Identify the blood parasite species.
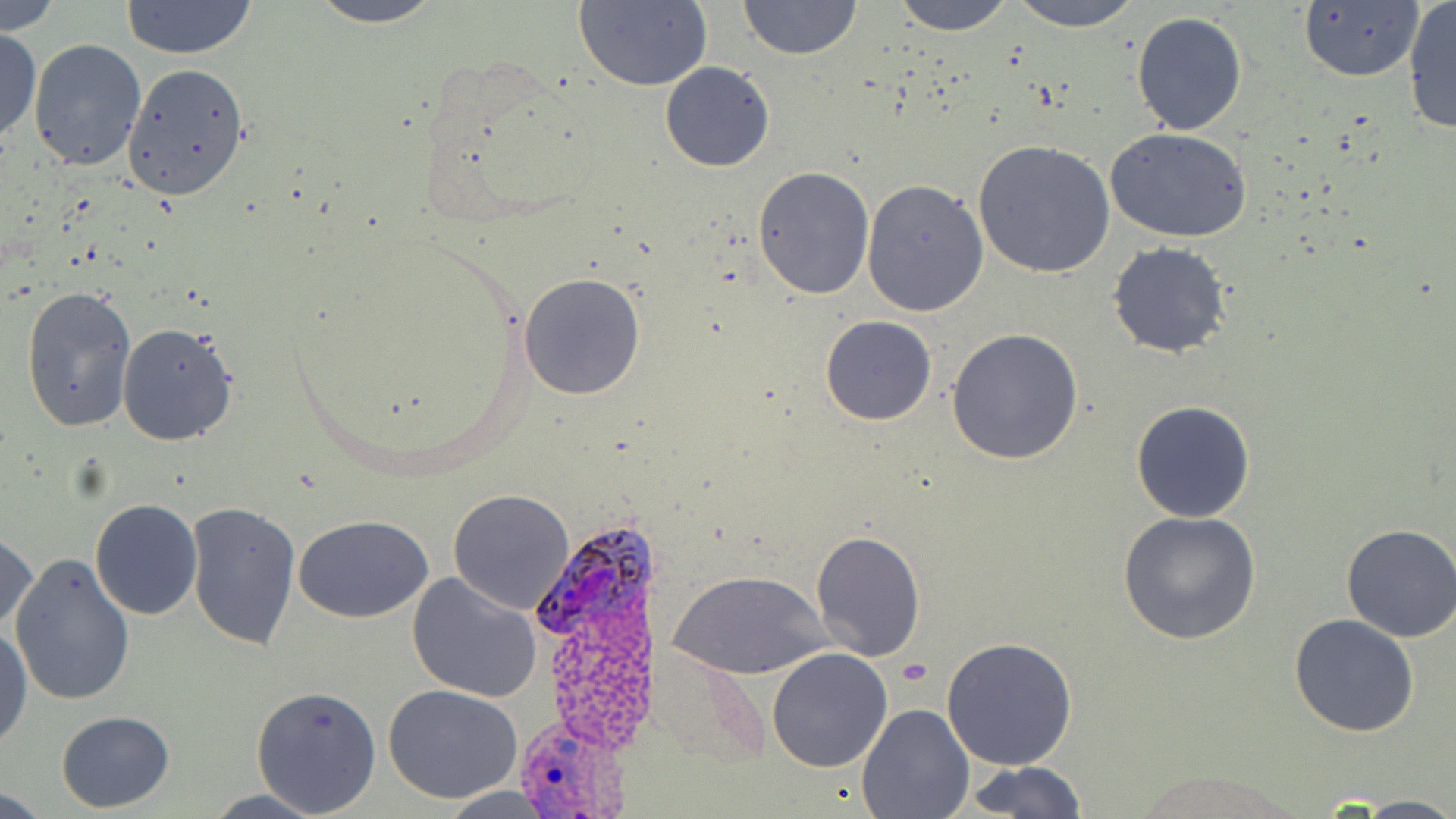
Plasmodium ovale.

{
  "stain": "May-Grünwald-Giemsa",
  "plasmodium_ovale_infected_red_blood_cell_locations": "approximate bounding boxes as named x1/y1/x2/y2 corners in pixels: (x1=534, y1=528, x2=655, y2=640), (x1=512, y1=716, x2=630, y2=819)",
  "image_size": "1456×819 pixels",
  "uninfected_red_blood_cell_locations": "approximate bounding boxes as named x1/y1/x2/y2 corners in pixels: (x1=119, y1=0, x2=259, y2=60), (x1=305, y1=0, x2=447, y2=28), (x1=892, y1=0, x2=1015, y2=36), (x1=1005, y1=0, x2=1146, y2=30), (x1=1, y1=1, x2=63, y2=35), (x1=738, y1=1, x2=862, y2=59), (x1=1402, y1=1, x2=1456, y2=136), (x1=573, y1=2, x2=713, y2=91), (x1=1297, y1=3, x2=1424, y2=84), (x1=1131, y1=10, x2=1248, y2=136), (x1=0, y1=27, x2=41, y2=147), (x1=27, y1=39, x2=146, y2=173), (x1=659, y1=61, x2=775, y2=172), (x1=120, y1=62, x2=251, y2=201), (x1=1107, y1=129, x2=1253, y2=242), (x1=971, y1=140, x2=1115, y2=279), (x1=752, y1=166, x2=874, y2=299), (x1=861, y1=180, x2=989, y2=315), (x1=1107, y1=241, x2=1233, y2=357), (x1=518, y1=273, x2=645, y2=400), (x1=21, y1=286, x2=138, y2=432), (x1=820, y1=315, x2=937, y2=425), (x1=116, y1=320, x2=239, y2=447), (x1=946, y1=328, x2=1083, y2=466), (x1=1131, y1=399, x2=1256, y2=522), (x1=447, y1=489, x2=575, y2=613), (x1=91, y1=498, x2=203, y2=619), (x1=185, y1=500, x2=301, y2=653), (x1=1118, y1=512, x2=1261, y2=646), (x1=294, y1=515, x2=434, y2=623), (x1=1338, y1=525, x2=1456, y2=642), (x1=1, y1=530, x2=38, y2=637), (x1=810, y1=531, x2=926, y2=661), (x1=9, y1=552, x2=134, y2=705), (x1=671, y1=568, x2=831, y2=678), (x1=406, y1=571, x2=545, y2=703), (x1=1289, y1=614, x2=1421, y2=736), (x1=0, y1=623, x2=31, y2=750), (x1=941, y1=637, x2=1077, y2=771), (x1=766, y1=647, x2=894, y2=773), (x1=249, y1=684, x2=381, y2=815), (x1=383, y1=684, x2=525, y2=805), (x1=856, y1=702, x2=975, y2=818), (x1=57, y1=711, x2=175, y2=811), (x1=962, y1=760, x2=1088, y2=819), (x1=1129, y1=767, x2=1305, y2=819), (x1=203, y1=790, x2=328, y2=819), (x1=1355, y1=795, x2=1456, y2=818)",
  "preparation": "thin blood smear",
  "modality": "light microscopy",
  "field_of_view": "one of a larger specimen",
  "magnification": "1000x",
  "platelet_locations": "approximate bounding boxes as named x1/y1/x2/y2 corners in pixels: (x1=896, y1=660, x2=931, y2=687)"
}